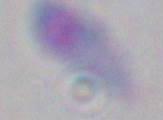
identification = Toxoplasma gondii
modality = micrograph
magnification = 1000x